Report the malaria status of this cell.
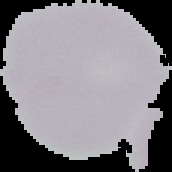
Uninfected.

Summary:
  - Image type: segmented cell region on a black background
  - Image size: 172×172 pixels
  - Preparation: thin blood smear